Give the position of every Plasmodium parasite visible.
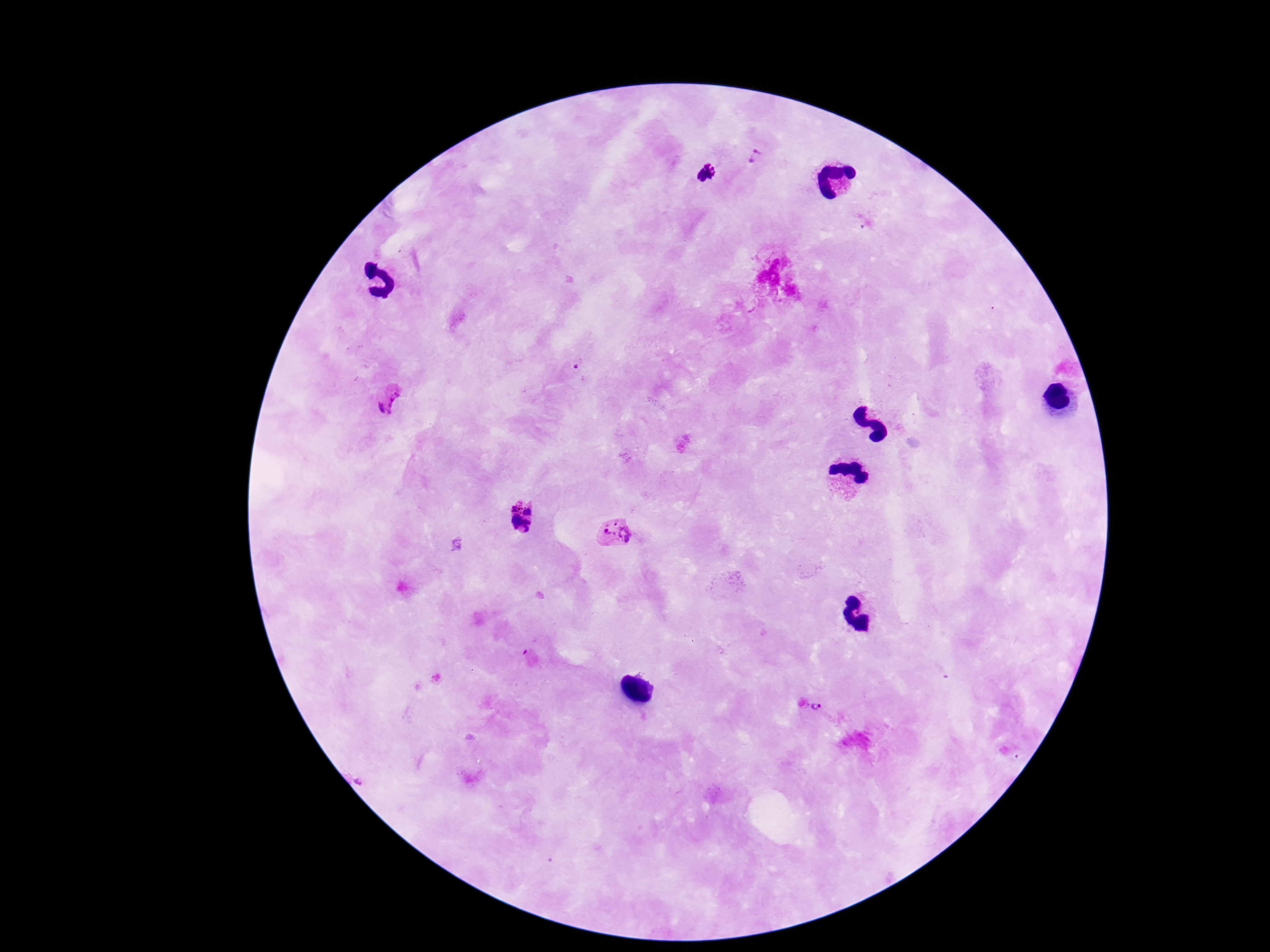
Approximate centers as [x, y] in pixels.
Plasmodium parasites: [758, 155], [706, 174], [393, 401], [525, 519], [614, 534], [455, 543], [815, 708].

Image is 1270×952 pixels. Single field of view. 100x magnification. Patient malaria status: infected. Photographed through the microscope eyepiece with a smartphone camera. Thick peripheral-blood smear. Giemsa-stained preparation.